Point out each Plasmodium parasite.
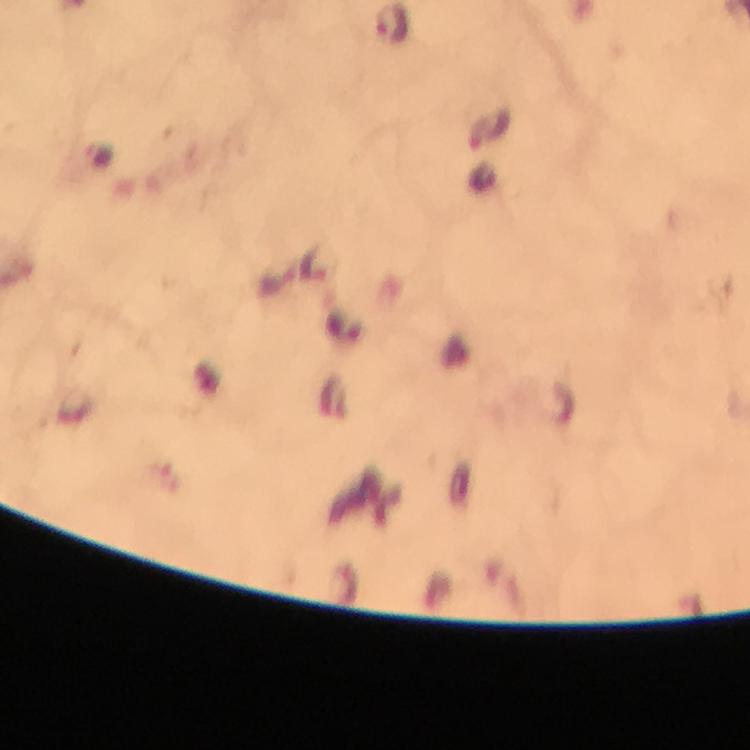

Approximate centers as [x, y] in pixels.
Plasmodium parasites: [392, 25], [491, 125].

{
  "cropped_from": "a single field of view",
  "context": "from a malaria diagnostic workup",
  "immersion_oil": "used",
  "stain": "Giemsa",
  "capture": "smartphone mounted on the microscope",
  "magnification": "100x",
  "image_size": "750×750 pixels",
  "preparation": "thick blood film"
}